Give the position of every Plasmodium parasite visible.
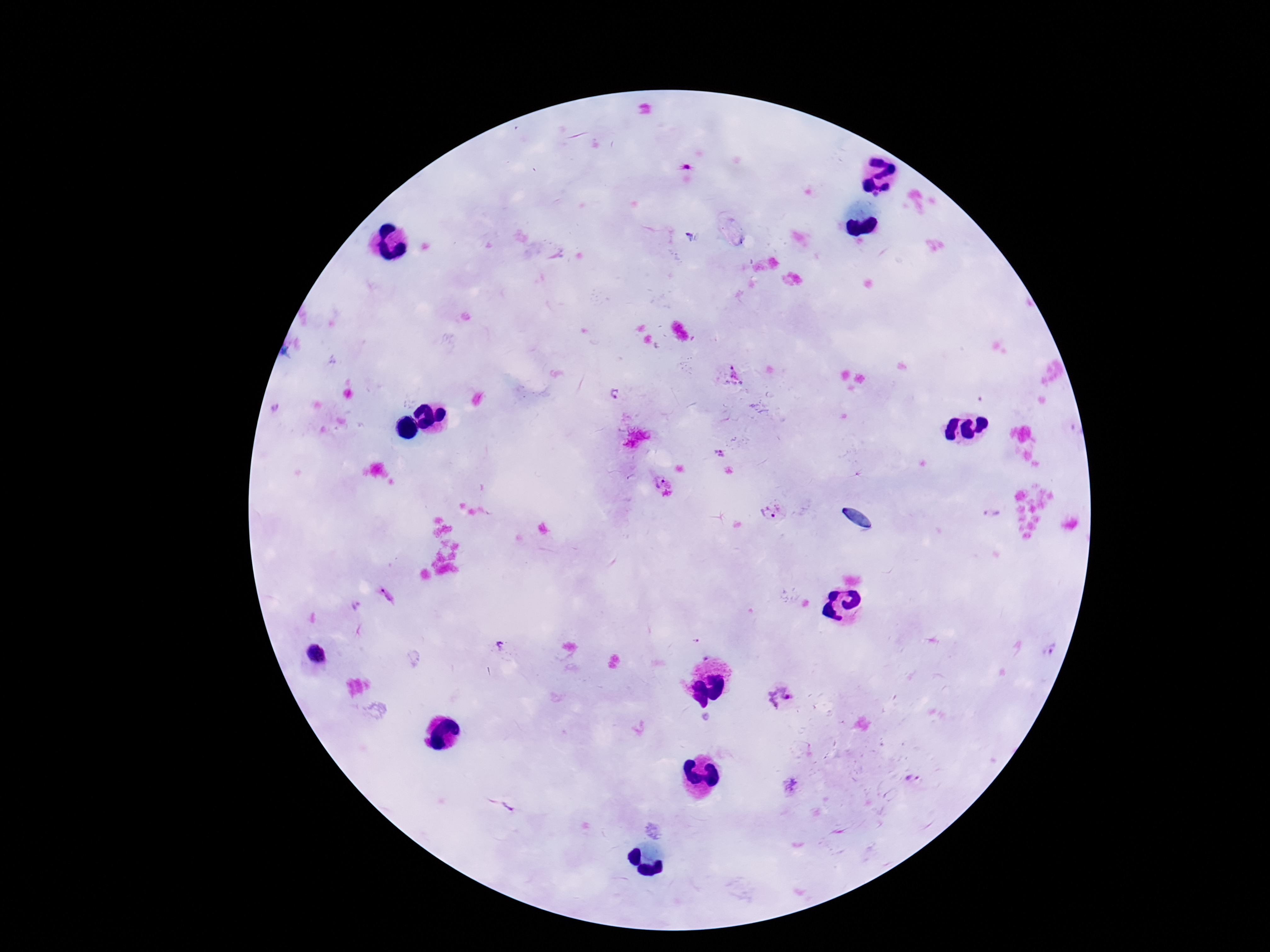
Approximate centers as {x, y} in pixels.
Plasmodium parasites: {614, 394}, {718, 453}, {661, 481}, {772, 514}, {993, 514}, {388, 595}, {1049, 650}, {780, 697}, {706, 719}, {911, 778}, {791, 785}, {508, 807}.

preparation = thick blood smear
stain = Giemsa
magnification = 100x
image size = 1270×952 pixels
patient malaria status = positive
capture = smartphone camera through the microscope eyepiece
field of view = single